Report the malaria status of this cell.
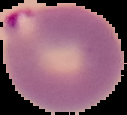
It is parasitized.

Summary:
  - Image type: segmented cell region on a black background
  - Preparation: thin blood smear
  - Image size: 127×115 pixels